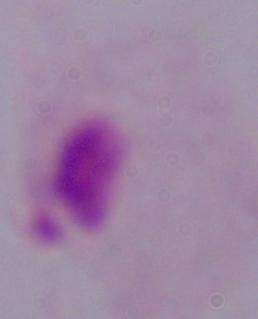

A trichomonad is seen. Captured at 1000x magnification. Micrograph.